State which parasite is depicted.
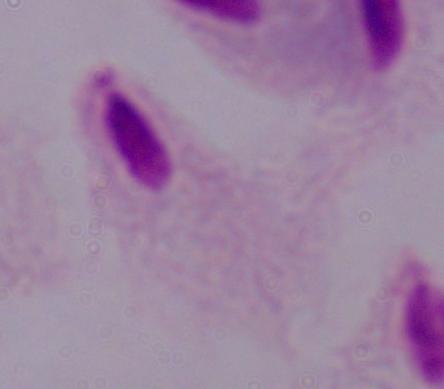

A trichomonad.

Photomicrograph. Captured at 1000x magnification.